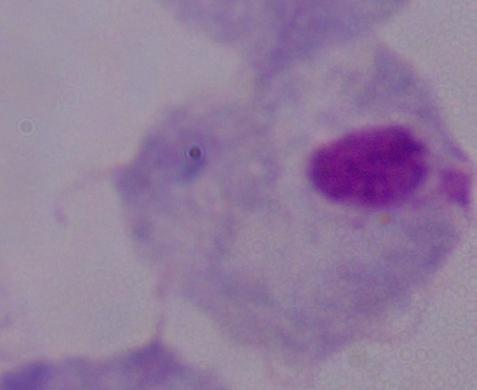
Summary:
  - Identification: trichomonad
  - Modality: photomicrograph
  - Magnification: 1000x